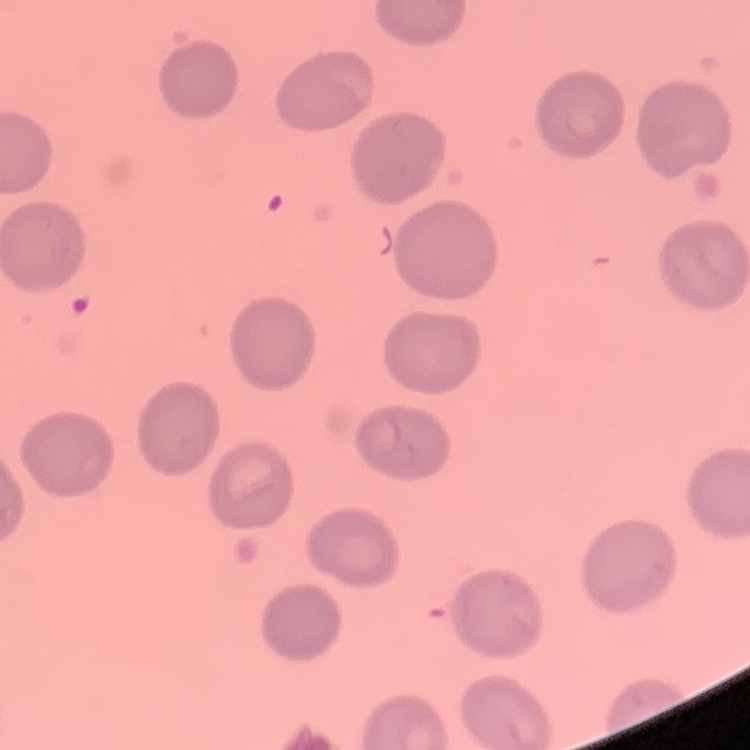
Summary:
  - Erythrocyte morphology: no rouleaux formation
  - Stain: Field's or Giemsa
  - Preparation: thin peripheral smear
  - Image type: one tile cut from a larger photomicrograph